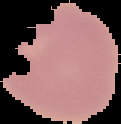

Summary:
  - Preparation: thin blood smear
  - Malaria status: uninfected
  - Image type: cell region segmented out of the field of view; surrounding area masked to black
  - Image size: 121×124 pixels